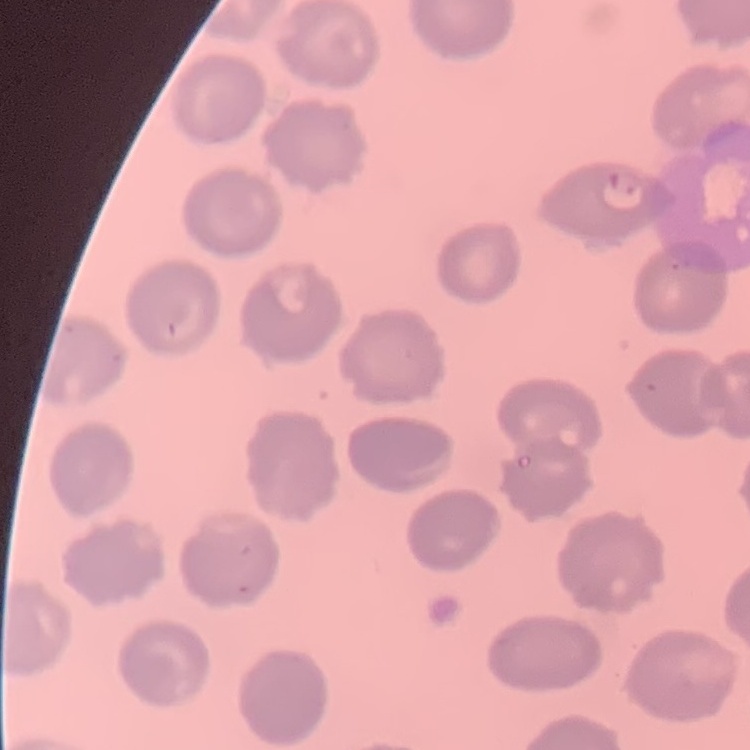

Summary:
  - Erythrocyte morphology: no rouleaux formation
  - Stain: Field's or Giemsa
  - Image type: one tile cut from a larger photomicrograph
  - Preparation: thin peripheral smear